Identify the parasite.
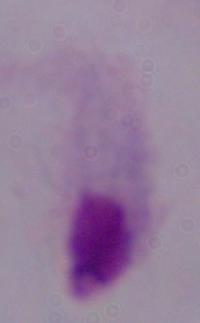
This is a trichomonad.

{
  "magnification": "1000x",
  "modality": "micrograph"
}